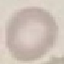

malaria status = uninfected
capture = smartphone through the microscope eyepiece
preparation = thin blood smear
image type = cell patch, automatically extracted from a larger field of view and resized to 64 × 64 pixels
stain = Giemsa